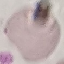

Malaria status: uninfected. Automatically extracted cell patch, resized to 64 × 64 pixels. Giemsa-stained preparation. Photographed with a smartphone camera at the microscope eyepiece. Thin blood film.